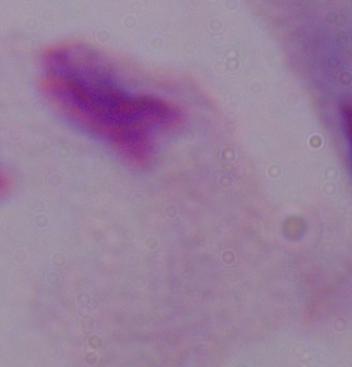
modality = photomicrograph
magnification = 1000x
identification = trichomonad